Assess this cell for malaria.
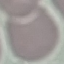
It is uninfected.

{
  "capture": "smartphone through the microscope eyepiece",
  "stain": "Giemsa",
  "image_type": "automatically extracted cell patch, resized to 64 × 64 pixels",
  "preparation": "thin blood film"
}